Report the malaria status of this cell.
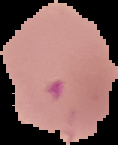

Parasitized.

Cell region segmented out of the field of view; the surrounding area is masked to black. Image is 118×145 pixels. From a thin blood film.